Outline platelets.
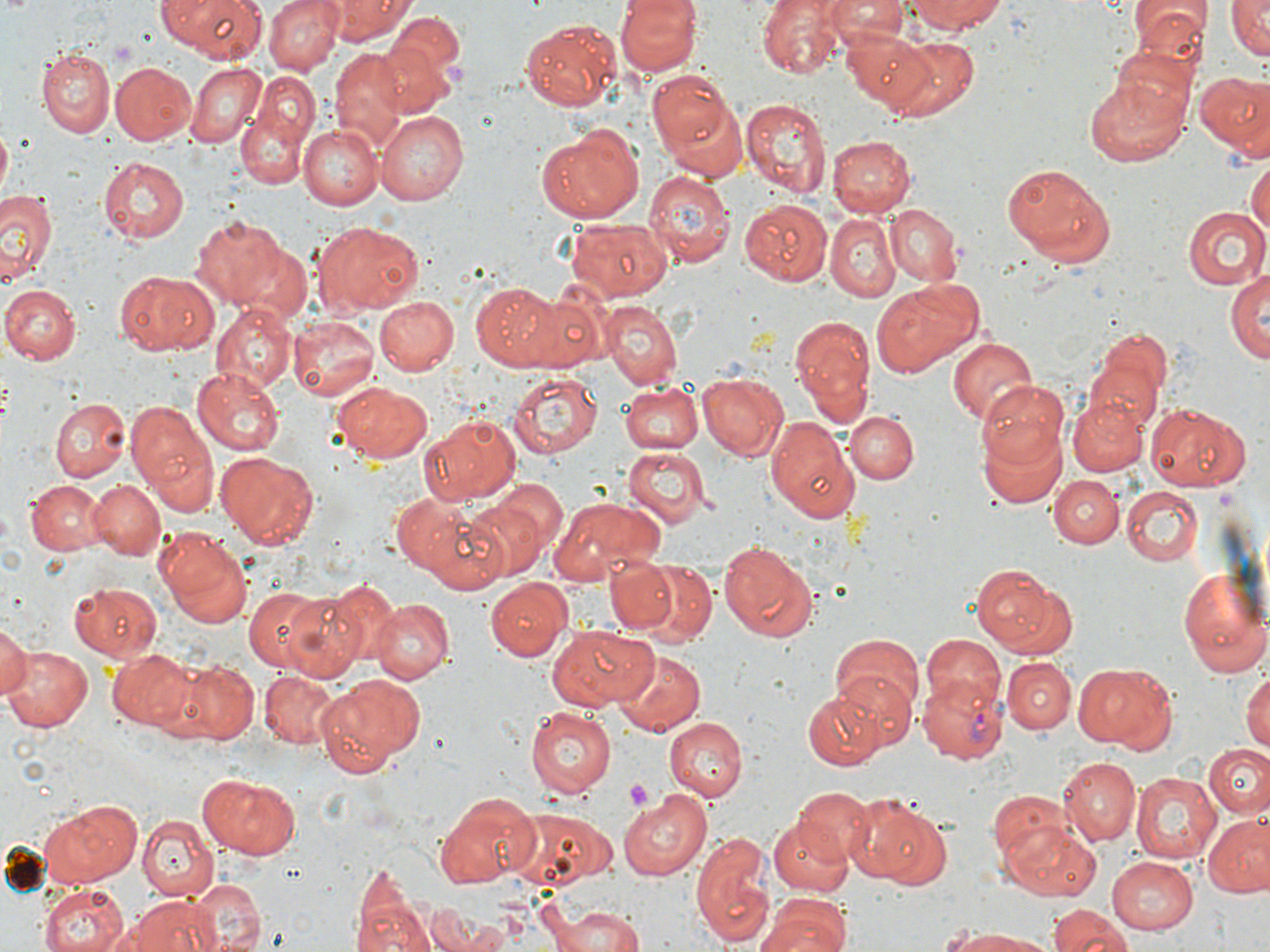

Approximate bounding boxes as (x1, y1, x2, y2) in pixels.
Platelets: (110, 41, 136, 64), (620, 778, 656, 815).

slide-level diagnosis = Plasmodium vivax
uninfected red blood cell locations = approximate bounding boxes as (x1, y1, x2, y2) in pixels: (158, 0, 265, 61), (265, 0, 345, 74), (326, 0, 412, 42), (616, 0, 701, 73), (757, 0, 848, 78), (822, 0, 907, 42), (905, 0, 1006, 37), (1225, 0, 1270, 61), (1129, 4, 1206, 78), (384, 7, 461, 85), (523, 19, 621, 108), (843, 30, 932, 111), (882, 37, 980, 119), (370, 41, 448, 118), (1108, 44, 1198, 133), (331, 49, 410, 133), (38, 50, 114, 136), (109, 61, 196, 144), (184, 62, 267, 149), (647, 67, 743, 166), (1195, 70, 1270, 154), (1082, 76, 1191, 166), (235, 80, 317, 189), (741, 98, 830, 195), (375, 111, 466, 204), (298, 124, 382, 209), (537, 127, 643, 222), (827, 136, 917, 217), (100, 155, 191, 242), (1247, 157, 1270, 245), (1004, 162, 1116, 267), (643, 170, 735, 269), (0, 186, 55, 286), (739, 199, 832, 285), (886, 203, 963, 285), (1184, 206, 1269, 288), (827, 216, 900, 299), (194, 217, 284, 306), (567, 218, 672, 301), (314, 223, 422, 314), (236, 245, 312, 323), (1227, 266, 1270, 367), (113, 270, 211, 354), (871, 280, 975, 376), (472, 282, 558, 367), (1, 284, 81, 363), (518, 293, 603, 370), (376, 297, 459, 377), (598, 301, 682, 385), (211, 303, 297, 390), (789, 313, 877, 417), (288, 315, 381, 401), (1090, 325, 1171, 422), (947, 337, 1037, 425), (1084, 362, 1160, 442), (192, 367, 286, 456), (508, 371, 602, 459), (698, 372, 787, 460), (978, 380, 1070, 470), (619, 381, 702, 454), (334, 383, 433, 462), (1068, 394, 1149, 477), (49, 396, 130, 480), (124, 400, 214, 511), (1145, 402, 1248, 490), (843, 411, 917, 483), (421, 414, 522, 504), (764, 414, 862, 523), (977, 421, 1070, 508), (623, 444, 710, 525), (218, 450, 319, 547), (1049, 475, 1123, 548), (27, 479, 103, 554), (490, 479, 568, 558), (91, 480, 164, 559), (1122, 486, 1202, 566), (460, 493, 553, 580), (555, 496, 664, 573), (407, 503, 513, 592), (153, 529, 252, 627), (716, 539, 819, 643), (1177, 562, 1270, 679), (604, 563, 680, 633), (975, 563, 1067, 656), (634, 567, 717, 647), (316, 579, 400, 669), (485, 580, 573, 662), (70, 583, 165, 662), (245, 587, 336, 671), (281, 589, 367, 678), (370, 598, 450, 682), (0, 622, 30, 704), (548, 623, 651, 710), (923, 633, 1003, 710), (831, 634, 924, 723), (2, 643, 92, 732), (109, 648, 196, 729), (612, 648, 706, 733), (1001, 654, 1077, 732), (163, 656, 259, 742), (1076, 662, 1177, 751), (1242, 668, 1270, 755), (833, 669, 917, 752), (260, 670, 339, 748), (314, 676, 417, 776), (802, 688, 886, 770), (526, 706, 621, 800), (663, 716, 747, 801), (1204, 743, 1270, 818), (1058, 756, 1139, 844), (196, 772, 300, 859), (1132, 772, 1226, 865), (794, 786, 873, 864), (989, 786, 1073, 870), (619, 789, 715, 881), (435, 793, 539, 889), (855, 797, 950, 892), (42, 798, 139, 887), (508, 806, 615, 885), (1202, 813, 1270, 897), (137, 814, 216, 899), (768, 817, 853, 896), (1004, 823, 1103, 902), (693, 833, 775, 948), (1105, 854, 1199, 934), (350, 868, 437, 952), (186, 879, 266, 951), (40, 883, 129, 952), (122, 895, 217, 952), (755, 896, 849, 952), (551, 903, 649, 950), (1047, 905, 1135, 952), (426, 906, 491, 952), (939, 926, 1055, 950)
modality = light microscopy
preparation = thin blood smear
magnification = 1000x
Plasmodium vivax-infected red blood cell locations = approximate bounding boxes as (x1, y1, x2, y2) in pixels: (917, 673, 1011, 762)
stain = May-Grünwald-Giemsa
field of view = single
image size = 1270×952 pixels